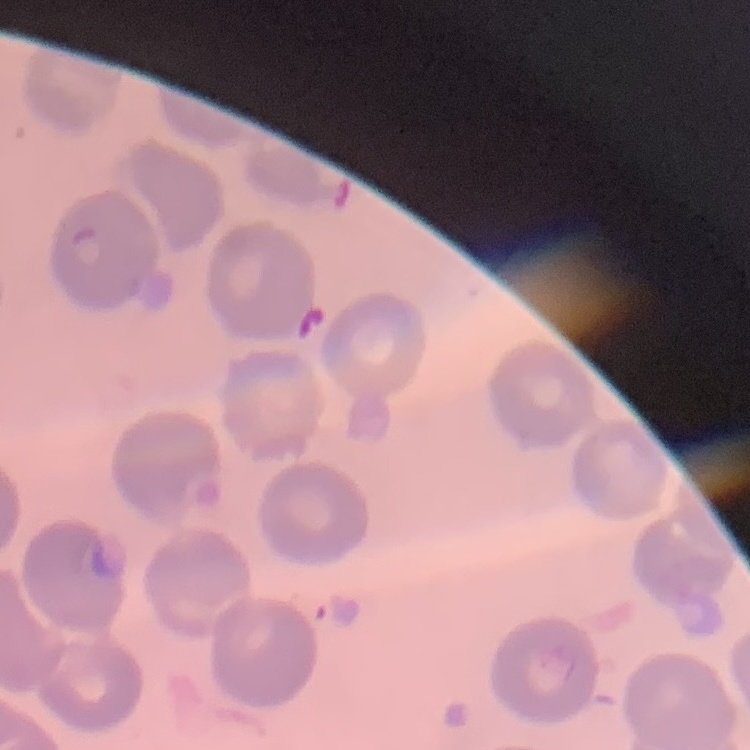
{
  "red_blood_cell_morphology": "no rouleaux formation",
  "preparation": "thin blood smear",
  "stain": "Field's or Giemsa",
  "image_type": "one tile cut from a larger photomicrograph"
}